Assess this cell for malaria.
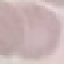

It is uninfected.

Giemsa stain. Automatically extracted cell patch, resized to 64 × 64 pixels. Photographed with a smartphone camera at the microscope eyepiece. Thin smear of blood.